Locate every blood parasite and identify its species.
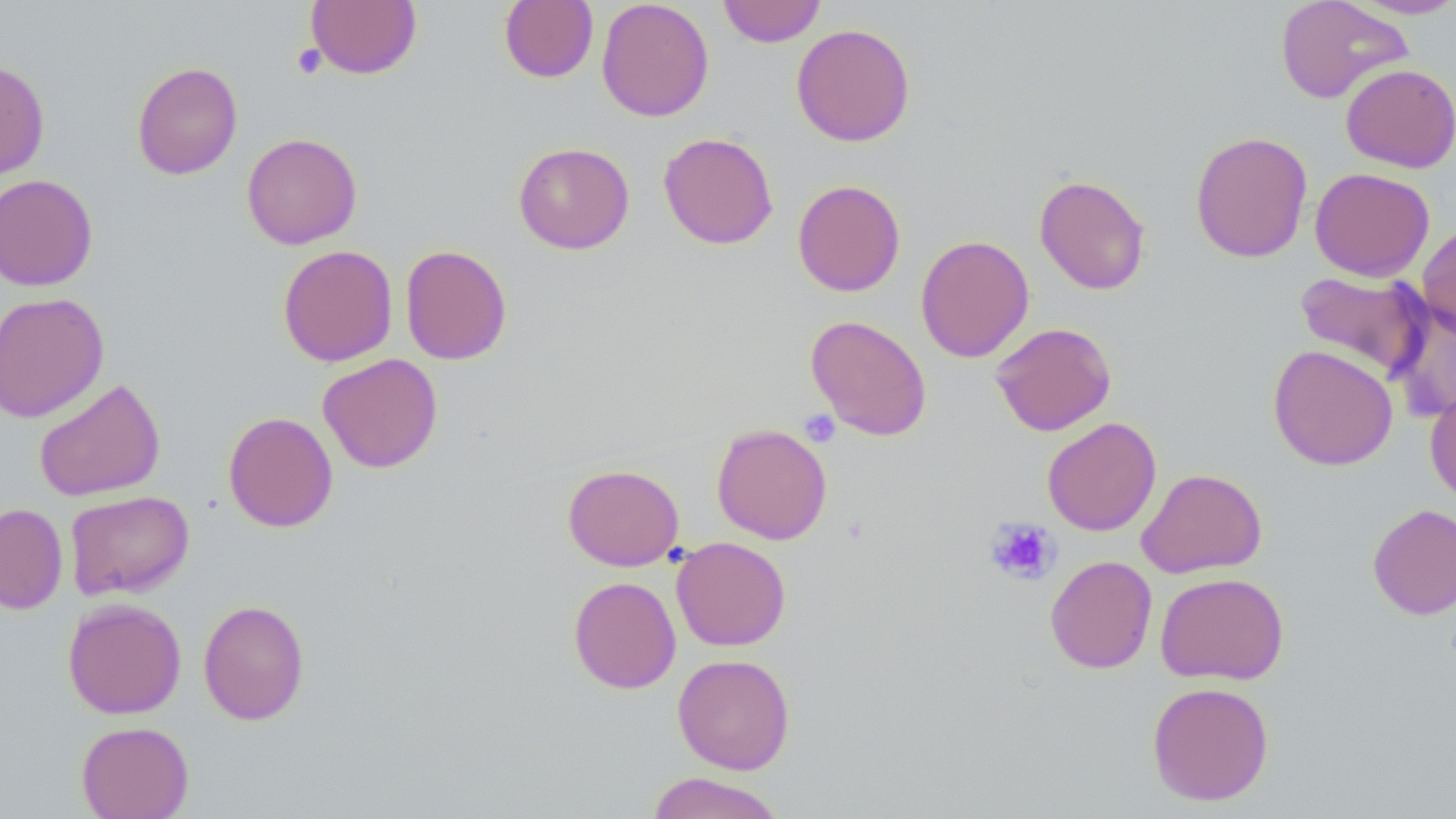

No blood parasites observed.

Summary:
  - Coordinate format: approximate bounding boxes as (x1,y1)-(x2,y2) corner pairs in pixels
  - Platelet locations: (292,43)-(327,79), (799,410)-(840,448), (985,518)-(1060,586)
  - Uninfected red blood cell locations: (305,0)-(422,79), (596,0)-(714,122), (717,0)-(827,47), (1274,0)-(1413,104), (499,1)-(598,83), (1348,1)-(1456,19), (791,23)-(915,146), (0,59)-(50,181), (131,61)-(243,180), (1340,63)-(1456,172), (1190,131)-(1313,263), (241,132)-(363,249), (658,132)-(779,250), (513,141)-(635,254), (1310,167)-(1435,281), (1,173)-(99,291), (1033,174)-(1151,295), (792,179)-(906,297), (1416,223)-(1456,338), (915,234)-(1034,363), (277,244)-(398,367), (399,244)-(512,365), (1294,269)-(1432,381), (0,292)-(109,423), (1387,300)-(1456,423), (805,315)-(932,441), (990,322)-(1116,436), (1268,343)-(1398,471), (317,353)-(442,473), (33,377)-(166,502), (1425,384)-(1456,504), (223,411)-(338,532), (1042,416)-(1161,536), (711,423)-(833,544), (563,463)-(684,571), (1136,468)-(1267,578), (65,490)-(194,600), (0,502)-(68,615), (1367,504)-(1456,619), (671,537)-(791,651), (1045,555)-(1157,673), (1154,572)-(1290,685), (568,576)-(681,694), (62,598)-(186,718), (198,599)-(310,725), (672,653)-(796,774), (1146,681)-(1275,806), (76,721)-(194,819), (646,772)-(786,819)
  - Slide-level diagnosis: negative for blood parasites
  - Preparation: thin blood film
  - Field of view: one of a larger specimen
  - Image size: 1456×819 pixels
  - Modality: optical microscopy
  - Stain: May-Grünwald-Giemsa
  - Magnification: 1000x